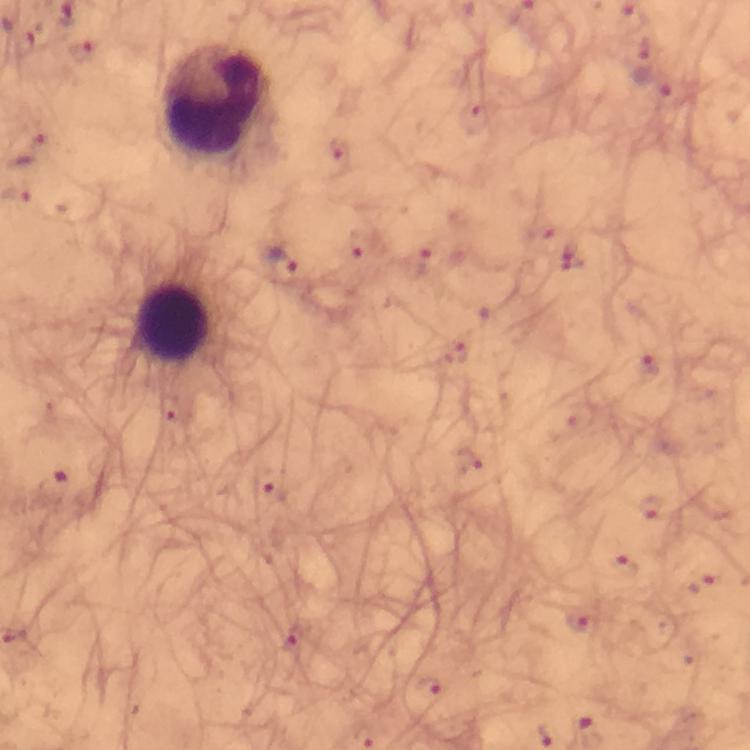

Approximate object centers, in pixels from the top-left corner.
Summary:
  - Plasmodium parasite locations: (x=84, y=55), (x=650, y=84), (x=30, y=150), (x=281, y=262), (x=54, y=485), (x=577, y=622), (x=429, y=688)
  - Leukocyte locations: (x=214, y=98), (x=172, y=322)
  - Context: from a malaria diagnostic workup
  - Image size: 750×750 pixels
  - Cropped from: a single field of view
  - Stain: Giemsa
  - Immersion oil: used
  - Preparation: thick smear
  - Capture: smartphone photograph through a microscope
  - Magnification: 100x